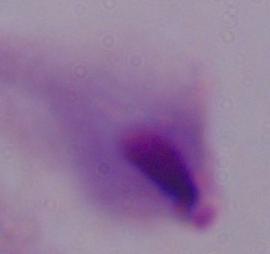

Captured at 1000x magnification. Micrograph. A trichomonad is seen.